Point out each Plasmodium parasite.
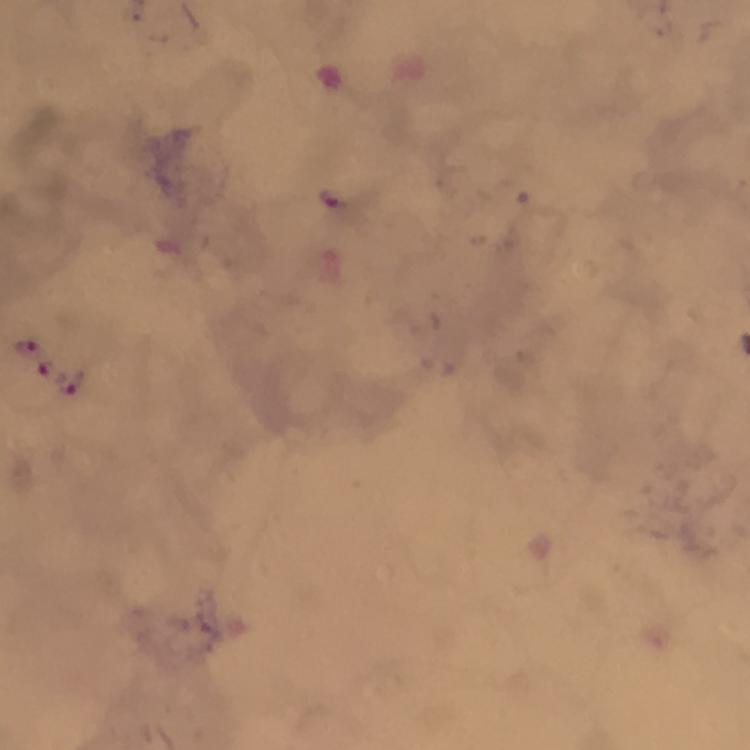
Approximate centers as {x, y} in pixels.
Plasmodium parasites: {330, 198}, {29, 348}, {73, 380}.

100x magnification. Smartphone photograph taken through a microscope. Image is 750×750 pixels. Thick smear. Cropped region of a single field of view. Giemsa-stained preparation. From a malaria diagnostic workup. Immersion oil was used.